Outline each blood parasite and name the species.
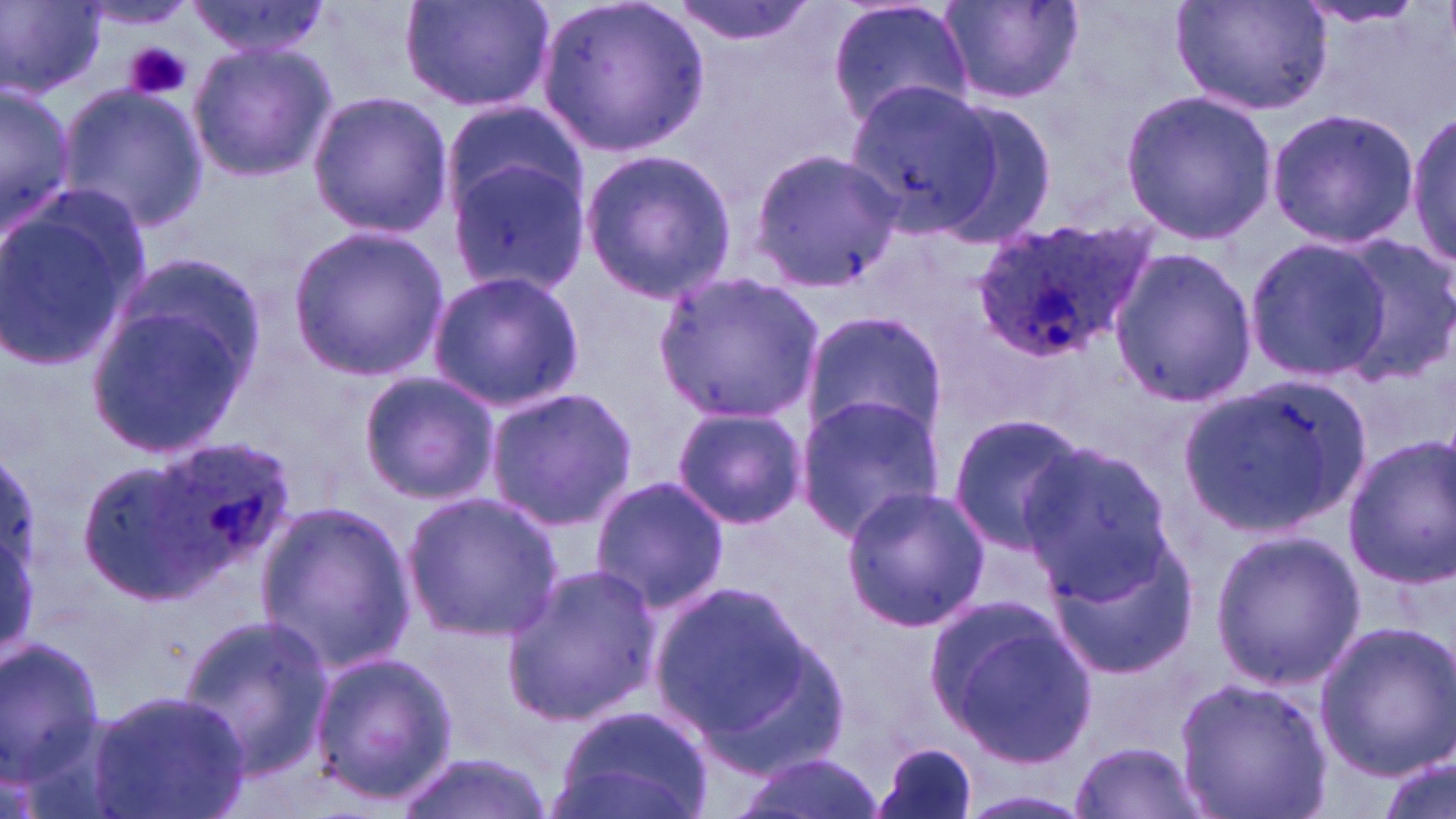

Approximate bounding boxes as (x1,y1)-(x2,y2) corner pairs in pixels.
Plasmodium ovale-infected red blood cells: (970,218)-(1147,362), (151,434)-(301,570).
No Plasmodium falciparum, Plasmodium malariae, Plasmodium vivax, Babesia divergens, or Trypanosoma brucei observed.

{
  "slide_level_diagnosis": "Plasmodium ovale",
  "magnification": "1000x",
  "stain": "May-Grünwald-Giemsa",
  "image_size": "1456×819 pixels",
  "preparation": "thin blood film",
  "modality": "light microscopy",
  "uninfected_red_blood_cell_locations": "approximate bounding boxes as (x1,y1)-(x2,y2) corner pairs in pixels: (2,0)-(106,98), (181,0)-(337,59), (397,0)-(557,116), (540,0)-(711,156), (666,0)-(818,49), (826,0)-(973,129), (939,0)-(1082,106), (1171,0)-(1333,119), (1293,2)-(1431,31), (186,36)-(337,185), (844,78)-(1004,238), (55,82)-(206,232), (1,86)-(76,234), (1120,89)-(1277,243), (306,92)-(452,237), (933,93)-(1062,246), (442,102)-(586,223), (1264,107)-(1420,249), (1407,108)-(1456,269), (751,147)-(899,290), (581,148)-(738,301), (445,152)-(590,296), (0,196)-(145,373), (288,224)-(449,381), (1245,236)-(1392,380), (1330,239)-(1456,382), (1108,249)-(1256,407), (425,269)-(585,414), (656,271)-(822,422), (84,287)-(261,459), (801,309)-(951,445), (356,371)-(498,503), (1178,371)-(1373,533), (484,386)-(637,532), (793,391)-(947,540), (670,406)-(807,531), (945,409)-(1088,550), (1340,435)-(1455,587), (1018,440)-(1177,599), (78,456)-(222,603), (590,476)-(730,612), (841,484)-(990,633), (401,490)-(562,642), (252,501)-(416,673), (1041,526)-(1199,679), (1210,528)-(1363,691), (500,562)-(663,729), (650,577)-(822,743), (929,596)-(1099,767), (177,614)-(334,786), (1314,620)-(1456,778), (0,636)-(107,786), (306,649)-(458,803), (1174,674)-(1332,819), (85,687)-(254,819), (549,704)-(718,819), (870,740)-(979,819), (1072,740)-(1205,818), (392,751)-(555,819), (735,752)-(882,819), (1377,755)-(1453,819), (960,791)-(1096,818)",
  "platelet_locations": "approximate bounding boxes as (x1,y1)-(x2,y2) corner pairs in pixels: (124,42)-(191,101)",
  "field_of_view": "single"
}